State which parasite is depicted.
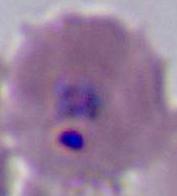

Plasmodium.

Captured at either 400x or 1000x magnification. Photomicrograph.